Describe the morphology of the erythrocytes.
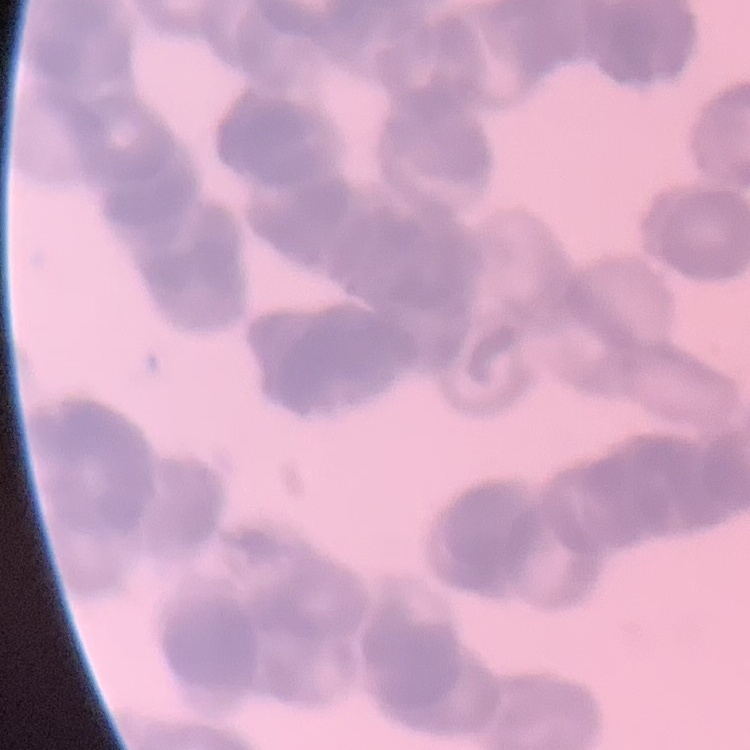
They show rouleaux formation.

preparation = thin blood film
image type = square crop of a larger photomicrograph
stain = Field's or Giemsa